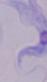

Summary:
  - Identification: trypanosome
  - Magnification: 1000x
  - Modality: micrograph